Identify the parasite.
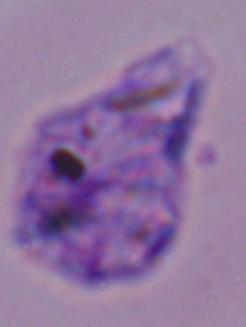
This is Leishmania.

Captured at 1000x magnification. Micrograph.